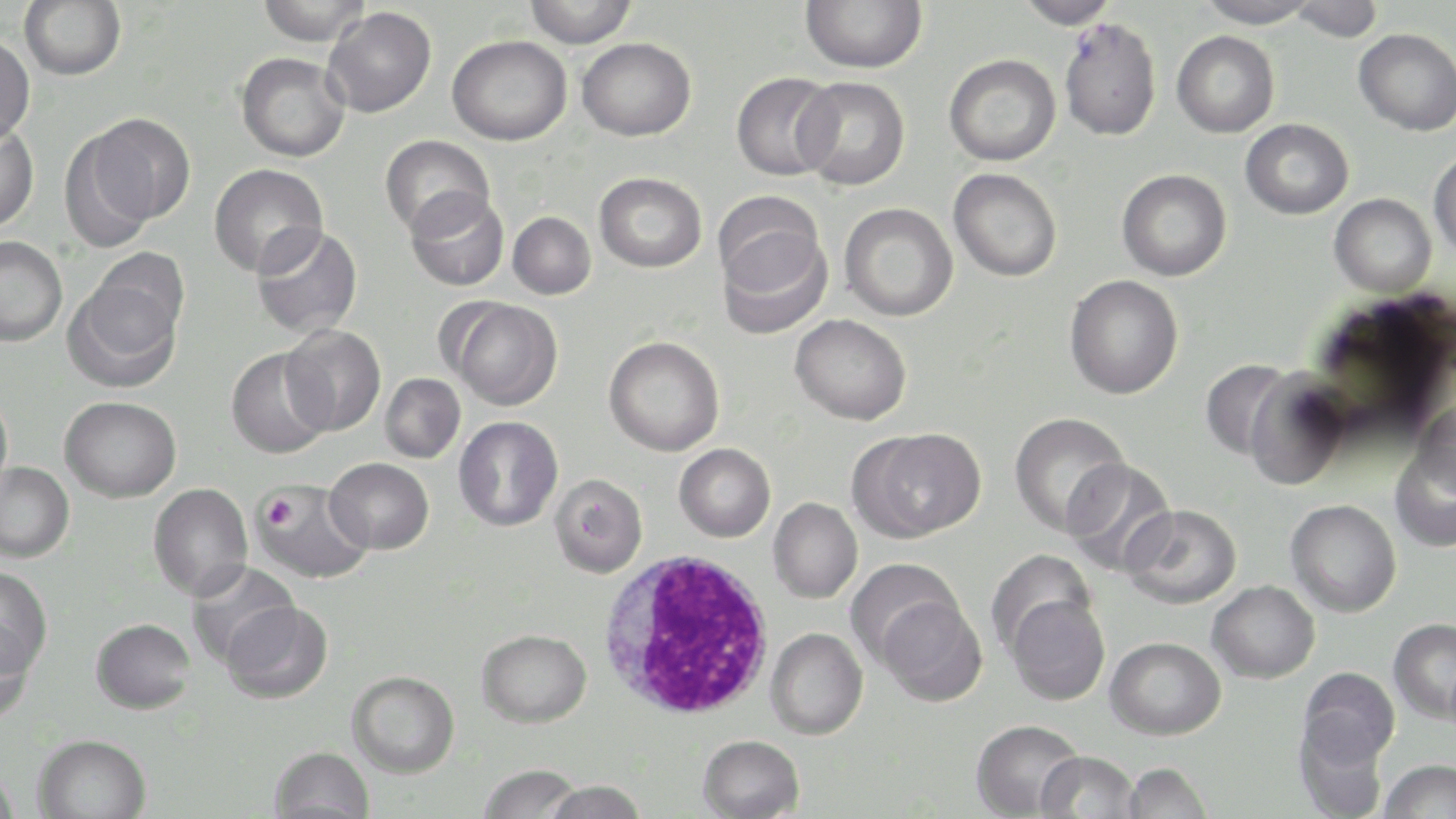
Approximate bounding boxes as (x1,y1)-(x2,y2) corner pairs in pixels. Uninfected red blood cell locations: (19,0)-(126,80), (254,0)-(372,46), (522,0)-(639,48), (800,0)-(927,73), (1016,0)-(1118,28), (1194,0)-(1320,28), (1287,0)-(1384,42), (323,7)-(436,118), (1059,17)-(1163,141), (1354,28)-(1456,135), (1172,31)-(1279,138), (0,34)-(36,145), (447,35)-(571,146), (577,37)-(696,141), (235,52)-(351,162), (944,53)-(1061,166), (731,71)-(841,181), (794,76)-(910,190), (86,113)-(197,225), (1240,118)-(1354,220), (0,120)-(39,231), (57,129)-(158,253), (379,134)-(494,239), (1428,148)-(1456,261), (208,163)-(328,277), (949,168)-(1062,282), (1116,168)-(1232,281), (594,172)-(707,273), (405,188)-(509,292), (1329,194)-(1437,298), (838,202)-(958,321), (714,203)-(832,336), (508,211)-(596,300), (251,223)-(363,339), (0,236)-(68,346), (86,247)-(191,352), (1064,275)-(1183,400), (64,276)-(183,393), (446,297)-(563,411), (790,314)-(912,425), (280,325)-(386,436), (603,336)-(725,456), (225,348)-(332,459), (1200,359)-(1295,461), (1244,369)-(1352,491), (380,373)-(465,463), (0,387)-(13,504), (60,396)-(181,503), (1412,400)-(1456,494), (1008,412)-(1131,538), (453,416)-(564,532), (852,427)-(986,542), (673,443)-(776,542), (1390,444)-(1456,552), (324,457)-(434,554), (1061,457)-(1178,576), (0,461)-(75,562), (549,474)-(648,578), (251,480)-(374,585), (148,483)-(253,601), (768,498)-(863,603), (1285,499)-(1402,617), (1120,504)-(1242,609), (988,549)-(1097,657), (844,558)-(964,667), (187,561)-(299,667), (0,567)-(52,678), (1207,580)-(1320,683), (1005,594)-(1110,706), (878,597)-(986,706), (221,601)-(333,704), (1388,617)-(1456,725), (90,618)-(196,714), (0,622)-(36,726), (765,627)-(868,739), (476,628)-(592,727), (1104,636)-(1226,740), (1298,667)-(1400,770), (347,670)-(460,778), (1293,717)-(1389,819), (971,719)-(1084,818), (32,733)-(152,819), (697,734)-(806,819), (268,746)-(375,819), (1035,750)-(1140,819), (1377,758)-(1455,818), (1122,761)-(1214,819), (477,764)-(586,818), (0,765)-(22,819), (543,780)-(650,819). Platelet locations: (265,499)-(304,532). White blood cell locations: (597,550)-(777,720). Slide-level diagnosis: Plasmodium falciparum. Captured at 1000x magnification. Image is 1456×819 pixels. One field of a larger specimen. Optical microscopy. May-Grünwald-Giemsa-stained preparation. Thin blood film.